Locate every Trypanosoma brucei.
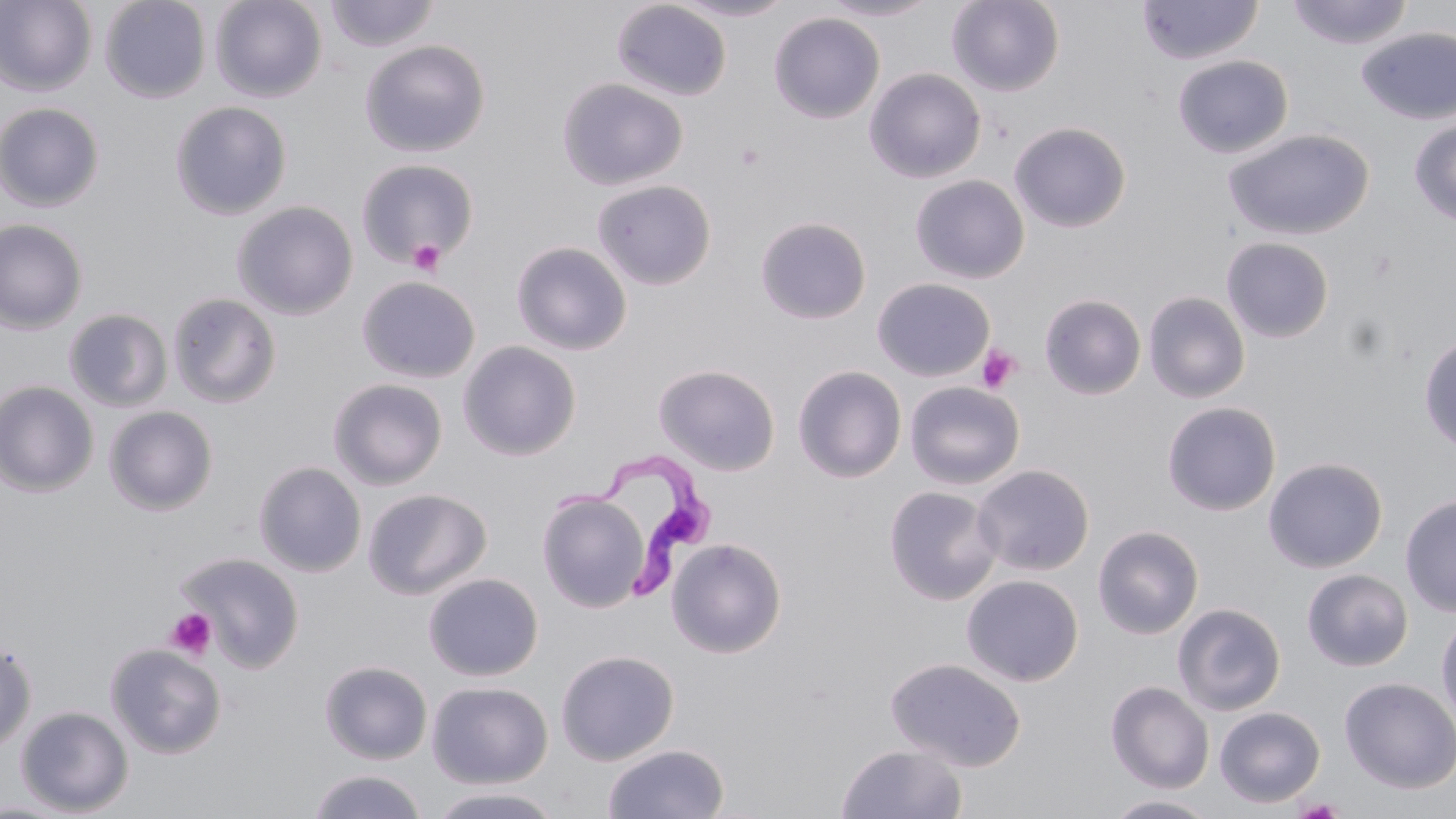

Approximate bounding boxes as (x1,y1)-(x2,y2) corner pairs in pixels.
Trypanosoma brucei: (552,451)-(716,605).

Platelet locations: (407,239)-(446,276), (977,345)-(1022,393), (164,608)-(216,661). Uninfected red blood cell locations: (0,0)-(97,97), (99,0)-(210,103), (210,0)-(327,103), (668,0)-(796,21), (818,0)-(940,21), (947,0)-(1065,96), (1136,0)-(1263,65), (1285,0)-(1415,49), (323,1)-(441,53), (612,1)-(732,101), (768,12)-(885,124), (1357,26)-(1456,124), (360,40)-(490,157), (1172,54)-(1293,159), (864,67)-(986,183), (557,77)-(688,190), (170,101)-(292,220), (0,102)-(105,212), (1408,118)-(1456,225), (1008,121)-(1132,233), (1224,128)-(1374,240), (357,158)-(479,268), (910,175)-(1030,284), (591,179)-(716,291), (232,201)-(358,320), (754,216)-(872,324), (0,219)-(88,334), (1221,237)-(1334,343), (510,241)-(632,355), (356,275)-(480,383), (872,278)-(995,382), (1143,291)-(1251,403), (167,292)-(282,409), (1040,294)-(1146,399), (63,309)-(173,412), (1419,335)-(1456,454), (458,340)-(581,461), (653,364)-(781,475), (792,366)-(907,482), (327,378)-(448,490), (0,380)-(99,497), (904,381)-(1025,490), (1162,402)-(1281,516), (104,405)-(219,515), (1263,457)-(1388,573), (253,462)-(367,577), (972,464)-(1094,577), (883,485)-(1003,605), (362,488)-(492,600), (536,491)-(651,612), (1400,493)-(1456,617), (1092,524)-(1204,639), (666,537)-(787,658), (176,551)-(304,672), (1302,569)-(1413,671), (423,572)-(544,681), (961,574)-(1084,687), (1172,603)-(1286,716), (1436,612)-(1456,733), (0,639)-(37,755), (105,643)-(227,759), (555,649)-(679,765), (886,657)-(1026,771), (319,660)-(433,765), (1338,677)-(1456,794), (427,681)-(553,789), (1106,681)-(1214,793), (15,705)-(134,816), (1214,706)-(1326,807), (603,743)-(729,819), (836,743)-(967,819), (307,770)-(429,819), (425,785)-(567,819), (1104,794)-(1220,818). Slide-level diagnosis: Trypanosoma brucei. Single field of view. Image is 1456×819 pixels. Light microscopy. 1000x magnification. May-Grünwald-Giemsa-stained preparation. Thin blood smear.